Give the position of every leukocyte visible.
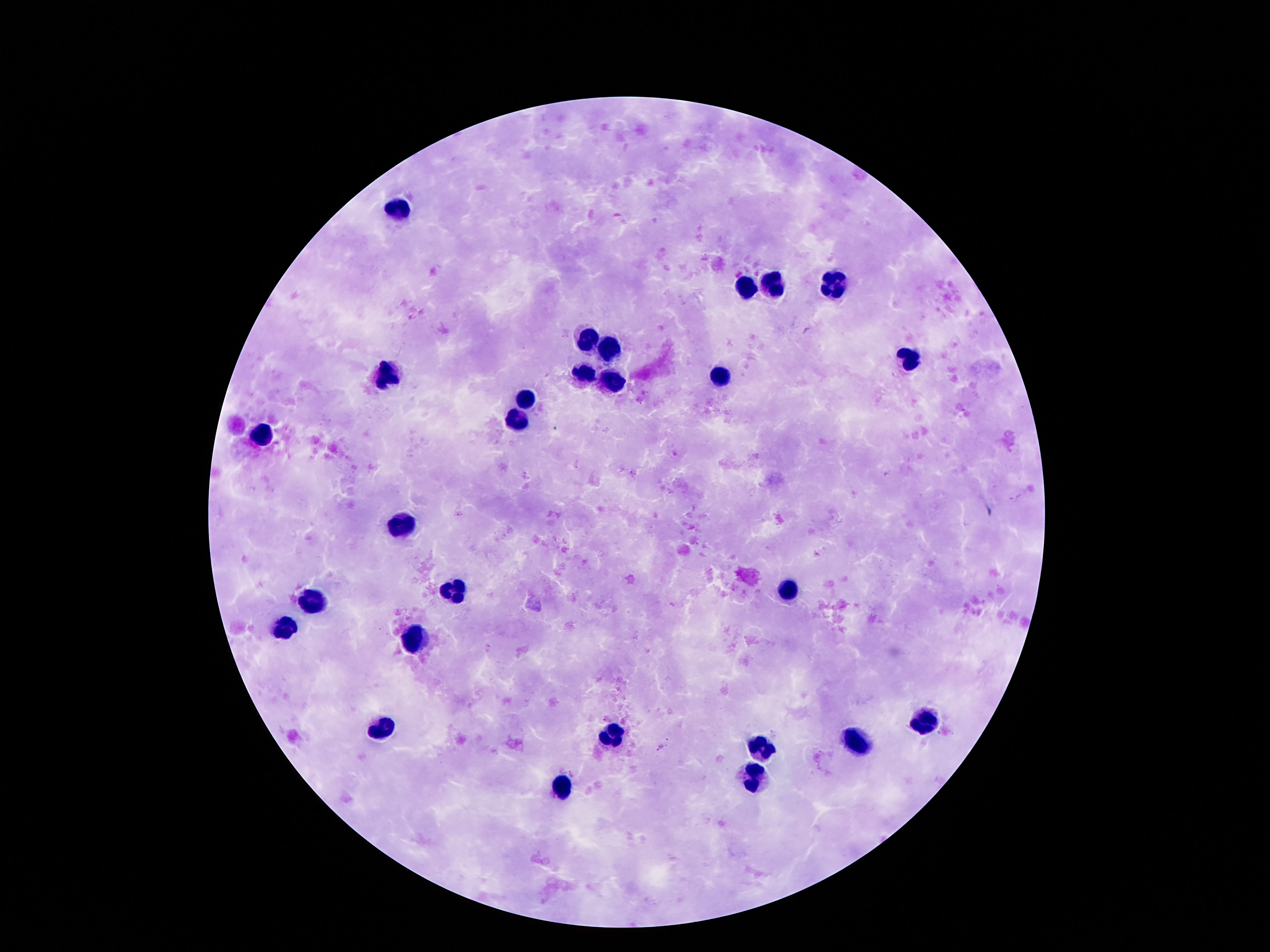
Approximate centers as (x, y) in pixels.
Leukocytes: (401, 206), (772, 284), (832, 287), (746, 290), (588, 341), (606, 350), (907, 357), (389, 374), (585, 375), (716, 379), (608, 384), (525, 398), (519, 417), (405, 523), (788, 590), (454, 591), (312, 603), (414, 639), (924, 720), (382, 729), (609, 734), (858, 741), (760, 746), (753, 777), (561, 790).

Summary:
  - Field of view: one from this slide
  - Stain: Giemsa
  - Capture: smartphone camera through the microscope eyepiece
  - Image size: 1270×952 pixels
  - Preparation: thick peripheral-blood smear
  - Patient malaria status: uninfected
  - Magnification: 100x